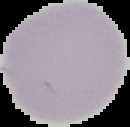

Summary:
  - Preparation: thin blood film
  - Image type: segmented cell region with the area outside set to black
  - Result: negative for malaria parasites
  - Image size: 130×127 pixels